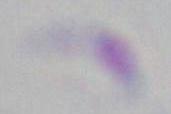
identification = Toxoplasma gondii
magnification = 1000x
modality = micrograph